Evaluate for Plasmodium parasites.
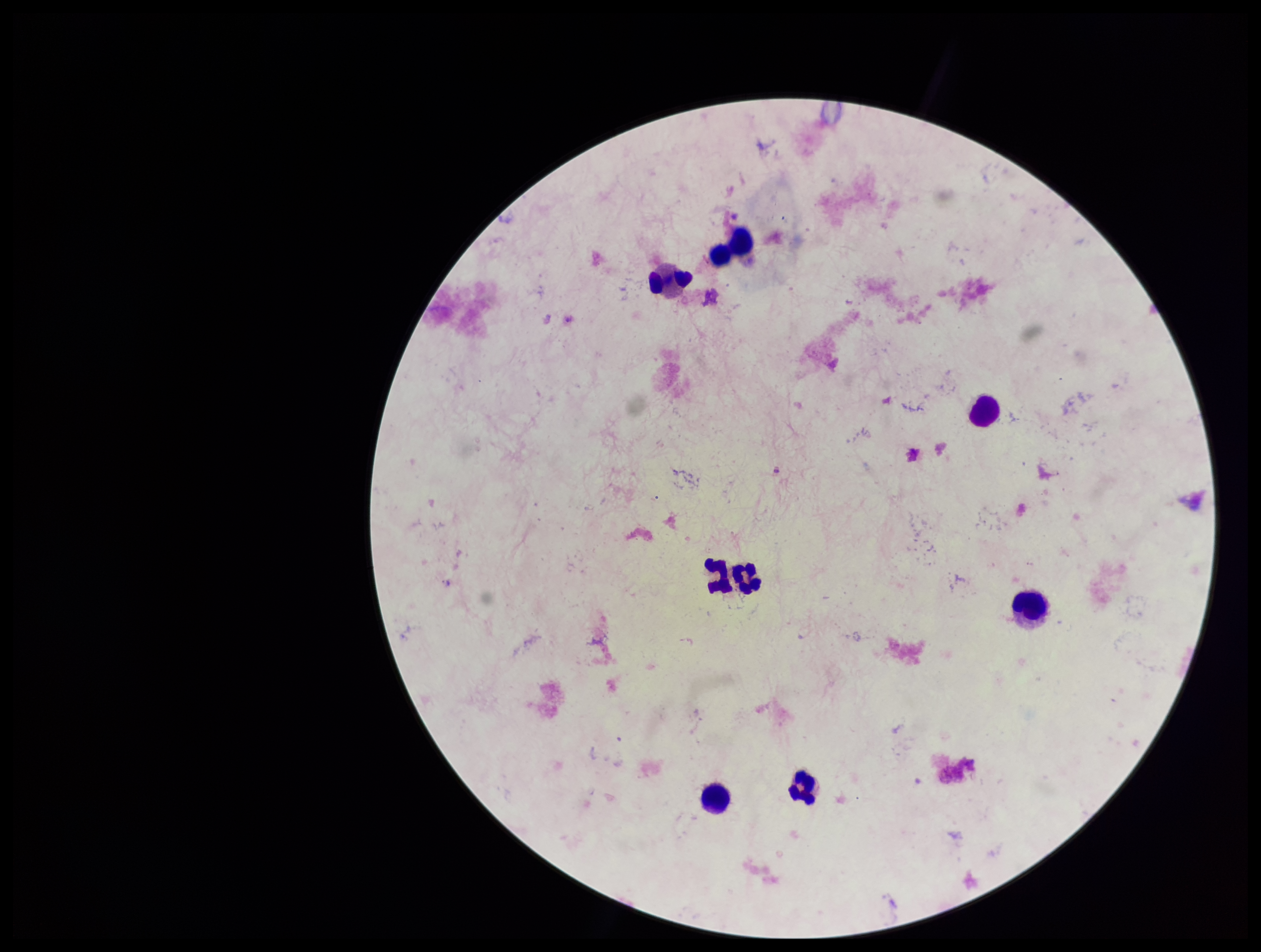
None detected.

Summary:
  - Image size: 1261×952 pixels
  - Stain: Giemsa
  - Field of view: one from this slide
  - Capture: smartphone photograph through the microscope eyepiece
  - Leukocyte count: 8
  - Parasite count: 0
  - Preparation: thick smear
  - Patient malaria status: negative